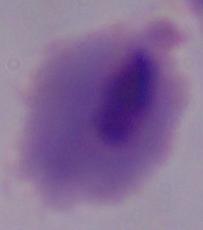 A trichomonad is seen. Photomicrograph. 1000x magnification.